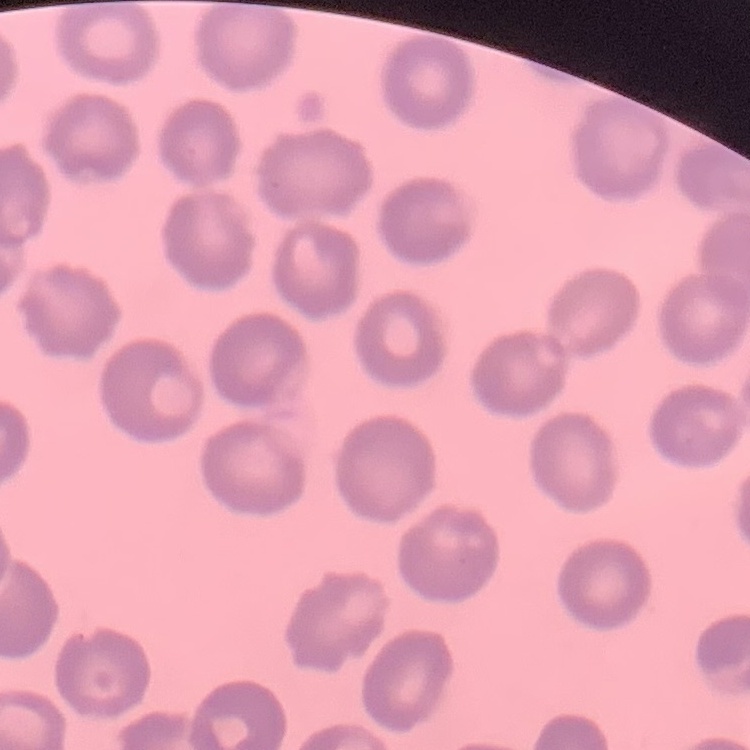

{
  "red_blood_cell_morphology": "no rouleaux formation",
  "preparation": "thin blood smear",
  "image_type": "one tile cut from a larger photomicrograph",
  "stain": "Field's or Giemsa"
}